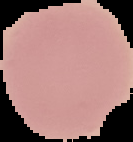

Summary:
  - Image size: 133×142 pixels
  - Result: no Plasmodium parasites seen
  - Image type: segmented cell region with the area outside set to black
  - Preparation: thin blood smear